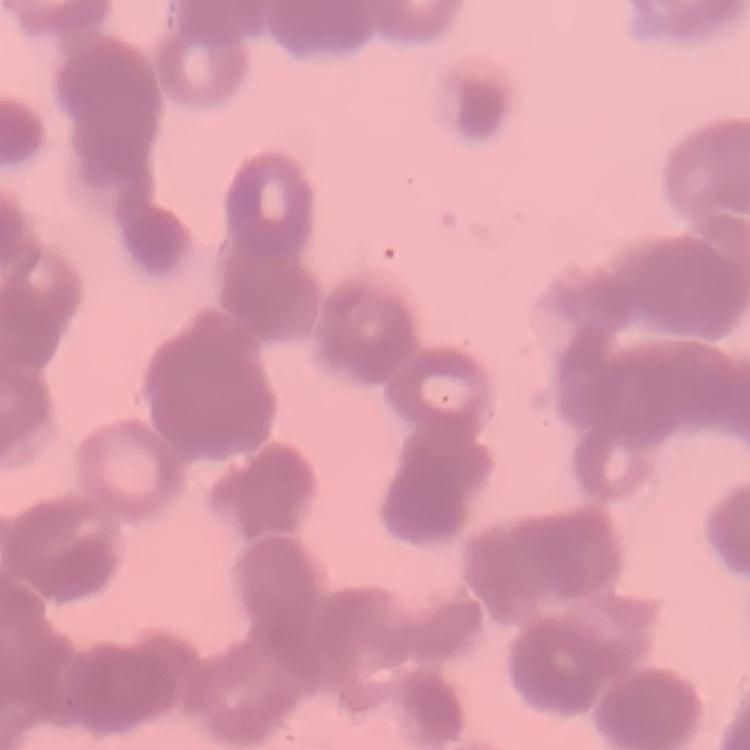

The erythrocytes exhibit rouleaux formation. Thin blood smear. Square crop of a larger photomicrograph. Field's or Giemsa stain.